Outline platelets.
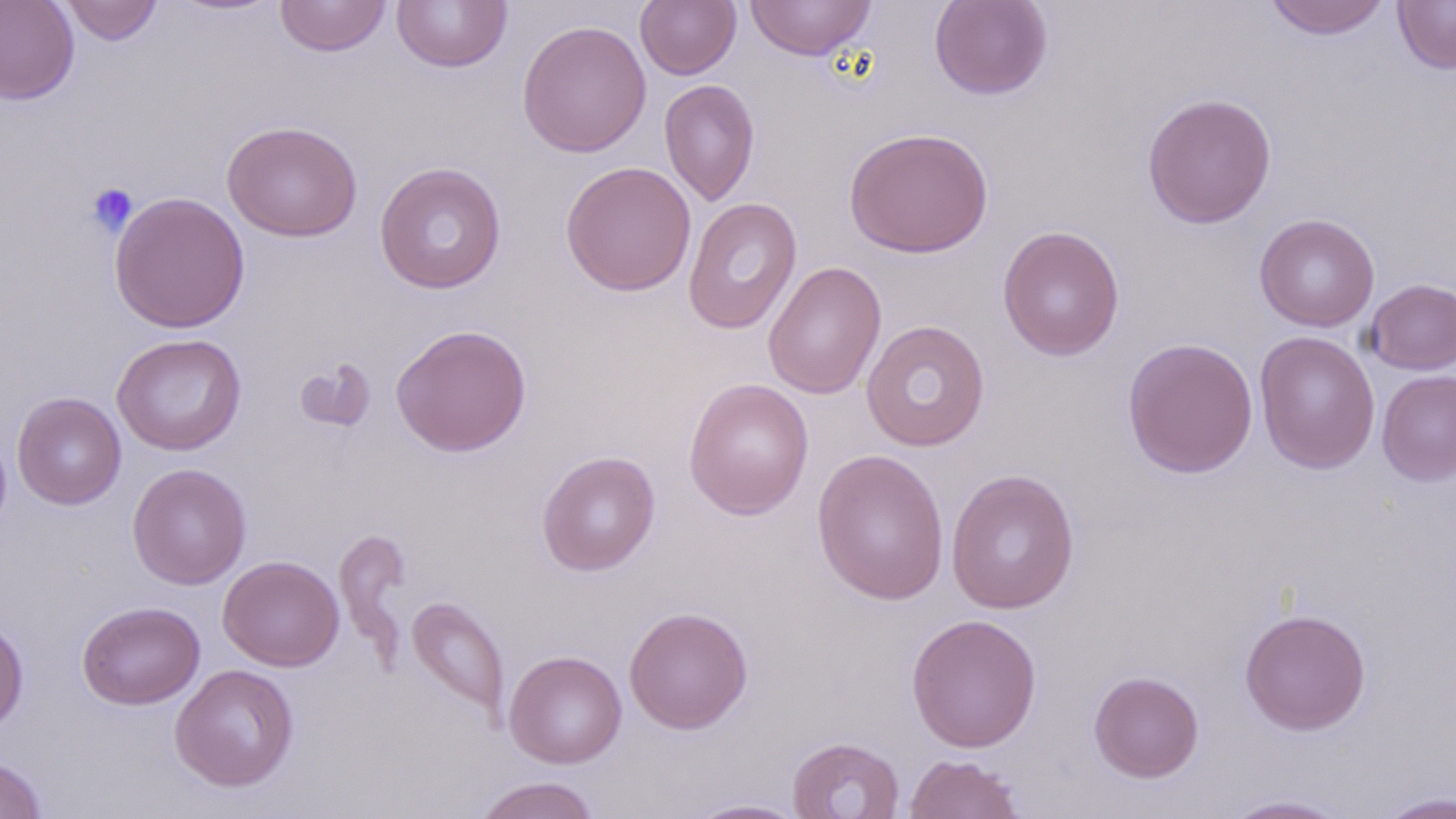

Approximate bounding boxes as (x1, y1, x2, y2) in pixels.
Platelets: (85, 182, 138, 236).

Uninfected red blood cell locations: (0, 0, 79, 105), (59, 0, 163, 45), (274, 0, 392, 57), (391, 0, 512, 73), (745, 0, 877, 62), (929, 0, 1054, 100), (1263, 0, 1392, 40), (1393, 0, 1456, 74), (635, 1, 741, 79), (517, 19, 652, 157), (659, 79, 760, 206), (1141, 92, 1277, 229), (222, 120, 363, 242), (844, 126, 994, 258), (560, 160, 696, 297), (374, 161, 507, 294), (109, 191, 250, 333), (683, 197, 802, 335), (1253, 213, 1380, 332), (997, 224, 1125, 362), (762, 260, 887, 400), (1365, 278, 1456, 374), (861, 319, 990, 452), (390, 323, 531, 457), (1254, 331, 1381, 474), (112, 333, 247, 456), (1122, 337, 1259, 479), (294, 357, 377, 435), (1377, 370, 1456, 485), (683, 377, 814, 520), (12, 392, 126, 509), (811, 447, 950, 605), (537, 450, 661, 575), (127, 463, 252, 590), (946, 468, 1080, 614), (333, 526, 412, 665), (218, 555, 344, 671), (406, 596, 510, 722), (77, 601, 205, 710), (624, 606, 753, 733), (1239, 608, 1371, 735), (0, 612, 29, 735), (905, 613, 1042, 753), (504, 650, 627, 769), (170, 664, 300, 792), (1089, 670, 1204, 782), (787, 736, 904, 819), (903, 753, 1026, 818), (0, 756, 49, 819), (472, 775, 601, 819), (1376, 790, 1456, 818), (1217, 794, 1356, 818), (683, 797, 811, 818). Slide-level diagnosis: negative for blood parasites. 1000x magnification. Image is 1456×819 pixels. Thin blood film. May-Grünwald-Giemsa stain. Light microscopy. One field of a larger specimen.